Describe the morphology of the red blood cells.
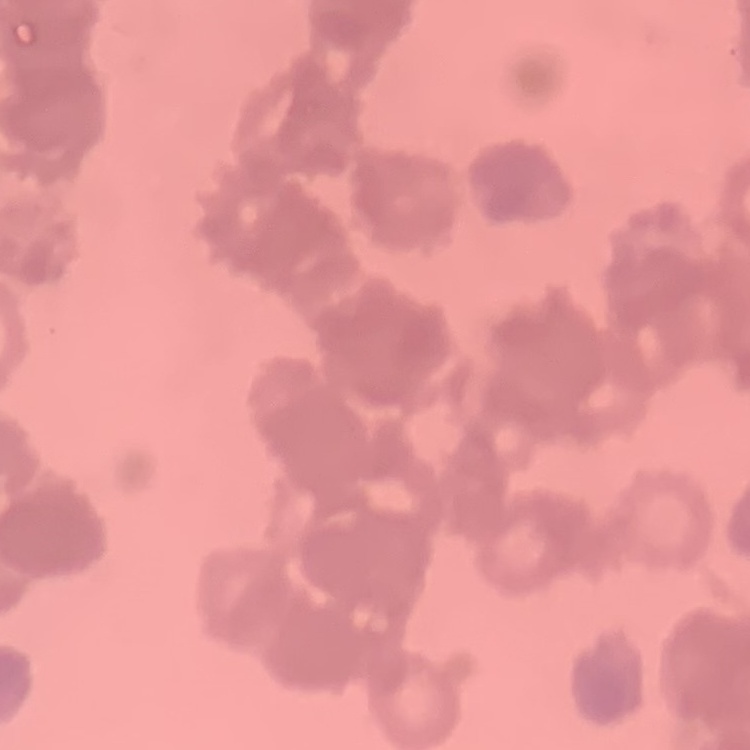
Rouleaux formation.

Square crop of a larger photomicrograph. Stained with either Field's or Giemsa. Thin peripheral smear.